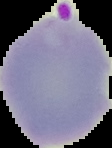

Image is 112×148 pixels. From a thin blood film. Result: malaria parasites identified. Cell region segmented out of the field of view; the surrounding area is masked to black.